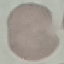

Summary:
  - Result: no malaria parasites detected
  - Image type: cell patch, automatically extracted from a larger field of view and resized to 64 × 64 pixels
  - Capture: smartphone camera at the microscope eyepiece
  - Preparation: thin smear
  - Stain: Giemsa